State the preparation type.
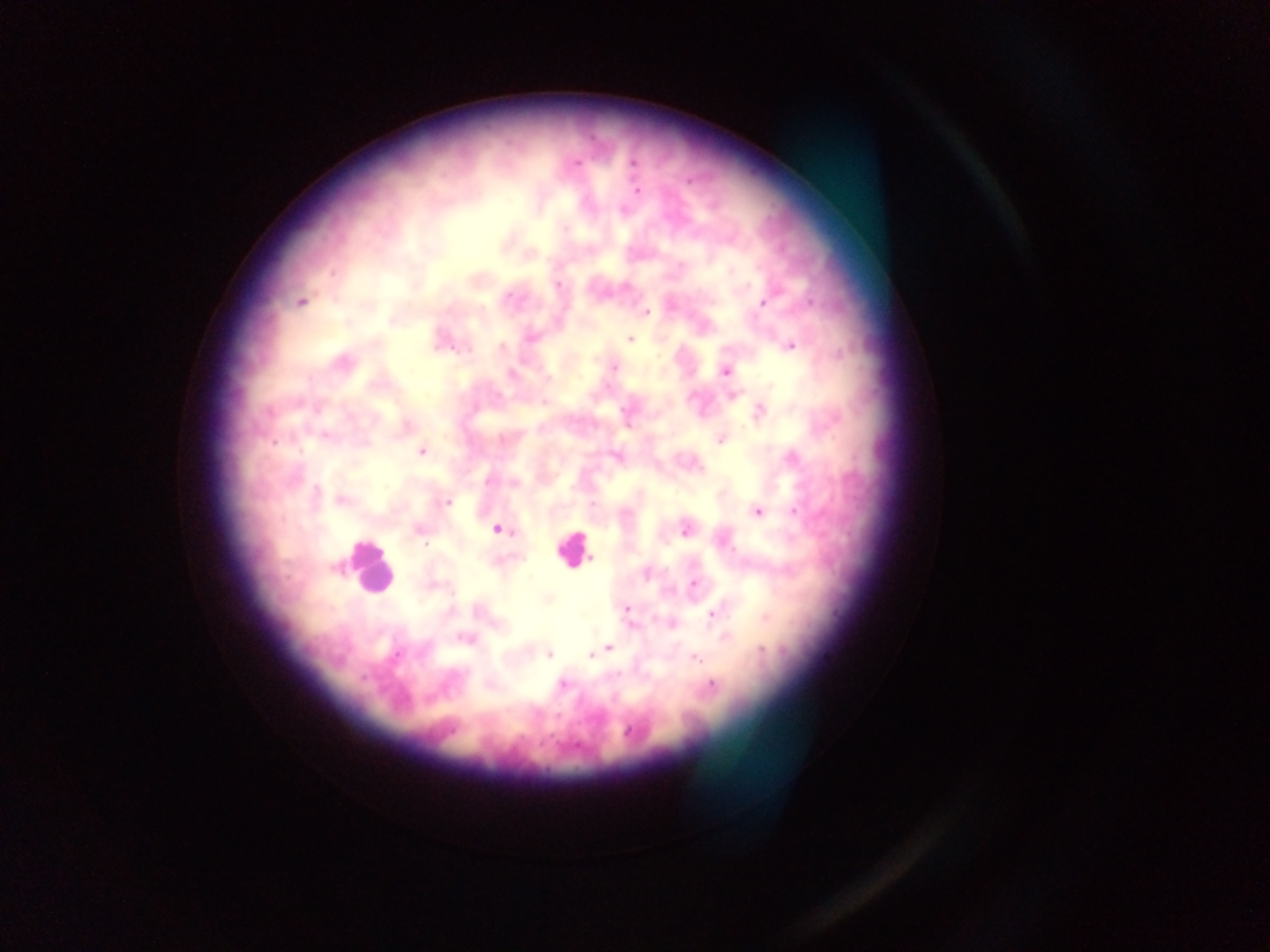

Thick blood smear.

malaria parasite locations = approximate centers as (x, y) in pixels: (633, 162), (577, 163), (637, 190), (565, 229), (732, 271), (332, 273), (558, 285), (626, 286), (509, 296), (300, 302), (764, 303), (811, 303), (646, 312), (531, 337), (630, 339), (791, 346), (502, 348), (467, 349), (615, 367), (727, 372), (511, 374), (545, 402), (761, 410), (720, 440), (274, 443), (421, 452), (793, 458), (488, 481), (341, 499), (447, 502), (593, 505), (796, 512), (757, 513), (497, 529), (685, 530), (425, 544), (591, 558), (647, 574), (695, 584), (626, 609), (713, 613), (670, 623), (632, 626), (724, 636), (463, 638), (608, 648), (597, 651), (549, 654), (396, 655), (591, 655), (696, 659), (617, 674), (562, 684), (712, 685), (558, 716), (628, 732)
country = Ghana
field of view = single
leukocyte locations = approximate centers as (x, y) in pixels: (572, 549), (369, 568)
capture = mobile-phone photograph through a microscope
image size = 1270×952 pixels